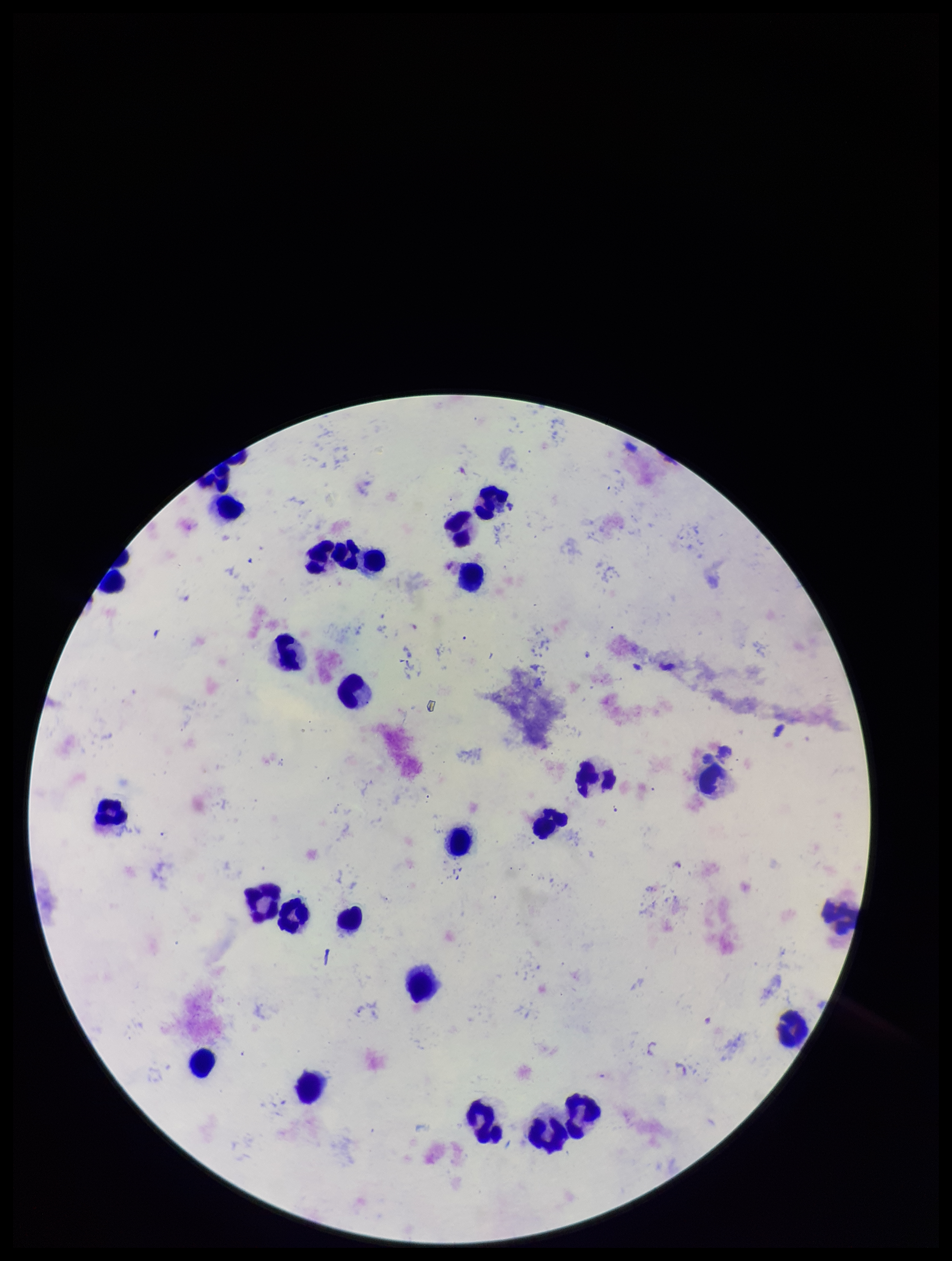

Patient malaria status: positive. Giemsa stain. Image is 952×1261 pixels. One field from this slide. Species reported for this patient: Plasmodium falciparum. Leukocyte count: 27. Preparation: thick. Parasite count: 1. Smartphone photograph taken through the eyepiece of a microscope. Plasmodium parasites: identified.